State which cell type is depicted.
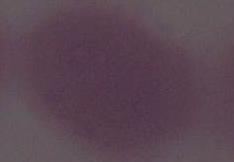

An erythrocyte.

Summary:
  - Modality: micrograph
  - Magnification: 1000x